Name the cell type shown.
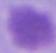

This is an erythrocyte.

Micrograph. Captured at 1000x magnification.